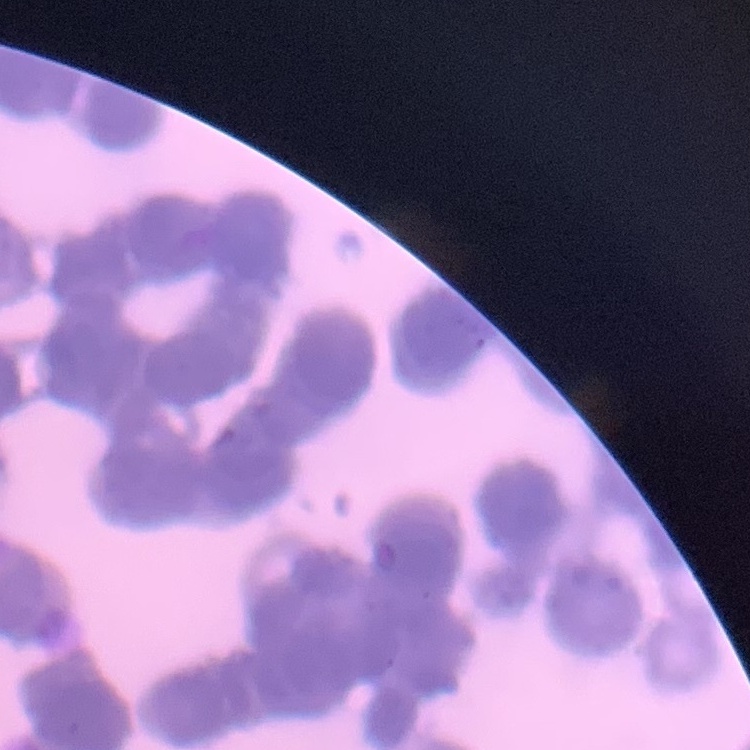
{
  "red_blood_cell_morphology": "rouleaux formation",
  "image_type": "square crop of a larger photomicrograph",
  "preparation": "thin blood film",
  "stain": "Field's or Giemsa"
}